State which cell type is depicted.
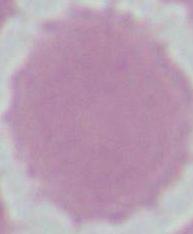
An erythrocyte.

Captured at 1000x magnification. Photomicrograph.